State the preparation type.
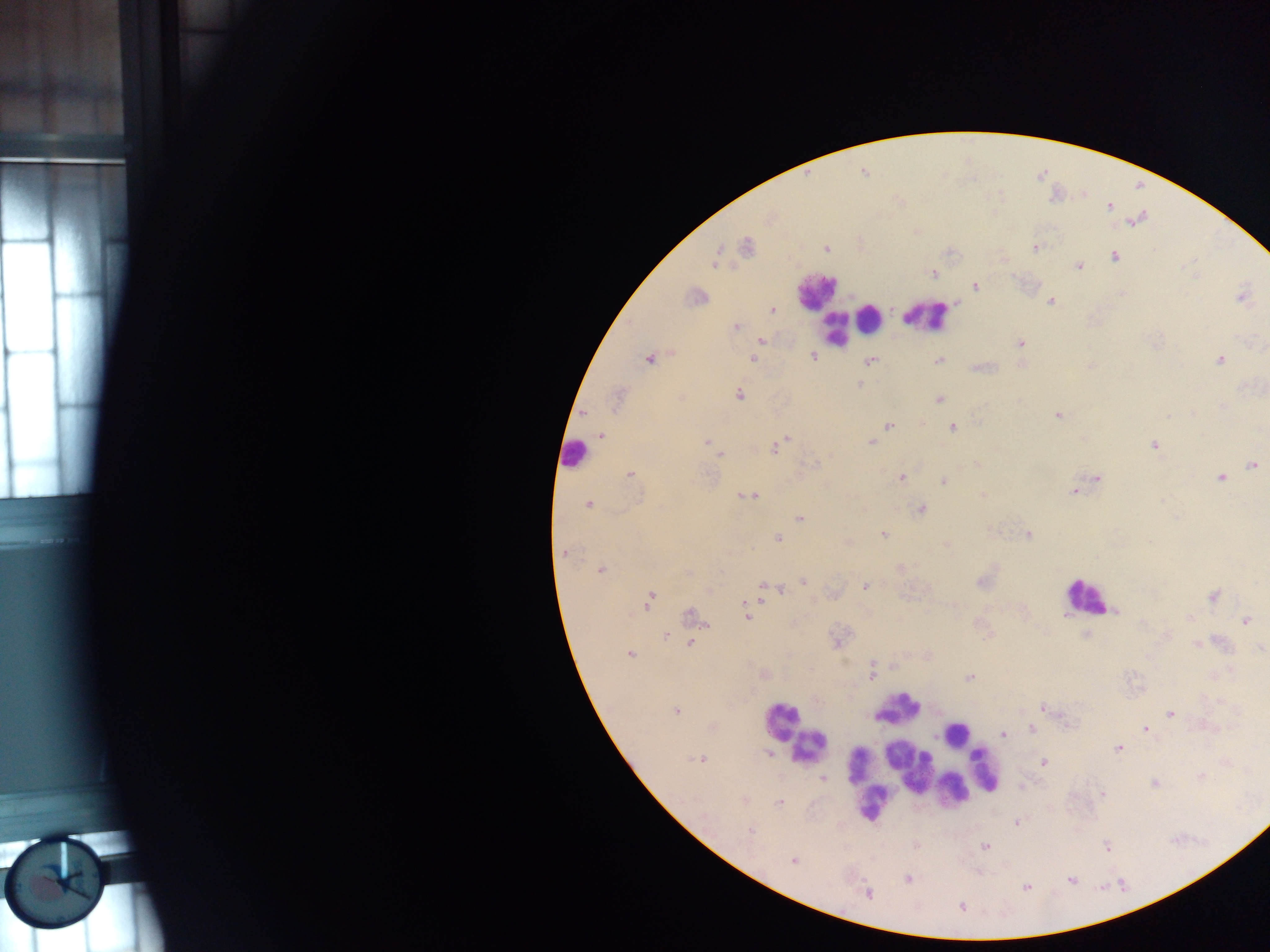

Thick blood smear.

Approximate centers as (x, y) in pixels. Malaria parasite locations: (1109, 206), (769, 219), (1136, 220), (746, 246), (1035, 248), (826, 249), (1115, 257), (715, 260), (1079, 265), (933, 273), (975, 286), (695, 297), (1242, 298), (1050, 301), (772, 310), (736, 327), (761, 341), (1020, 343), (813, 356), (649, 358), (752, 359), (1220, 359), (939, 360), (871, 361), (1091, 365), (983, 367), (859, 384), (739, 395), (618, 399), (939, 399), (1058, 415), (889, 425), (952, 427), (601, 435), (785, 440), (707, 442), (870, 443), (1155, 445), (775, 447), (714, 448), (719, 453), (978, 465), (1253, 466), (631, 474), (901, 478), (1096, 478), (1220, 478), (943, 480), (1074, 491), (743, 495), (983, 495), (752, 496), (588, 505), (922, 509), (800, 518), (883, 533), (1027, 534), (778, 539), (564, 553), (901, 568), (600, 570), (688, 572), (803, 581), (981, 582), (865, 586), (770, 587), (781, 590), (1213, 596), (650, 599), (1115, 611), (692, 615), (747, 617), (1246, 621), (666, 636), (690, 644), (1196, 644), (630, 654), (892, 667), (764, 674), (871, 675), (969, 677), (1044, 708), (677, 712), (1171, 713), (1033, 729), (1146, 729), (1004, 734), (1118, 748), (768, 753), (699, 759), (1044, 762), (1200, 776), (823, 779), (1154, 783), (1102, 794), (744, 801), (779, 802), (1017, 823), (750, 831), (985, 846), (1107, 846), (794, 860), (908, 879), (1071, 880), (1026, 888), (868, 893), (962, 907). Leukocyte locations: (817, 290), (926, 315), (870, 317), (835, 330), (574, 455), (1085, 596), (899, 709), (780, 721), (955, 733), (808, 747), (908, 766), (985, 769), (953, 790), (870, 803). Mobile-phone photograph taken through the microscope. Sample from Ghana. Image is 1270×952 pixels. Single field of view.